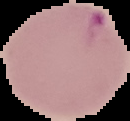
The area outside the segmented cell region is set to black. Malaria status: parasitized. Image is 130×121 pixels. From a thin blood smear.